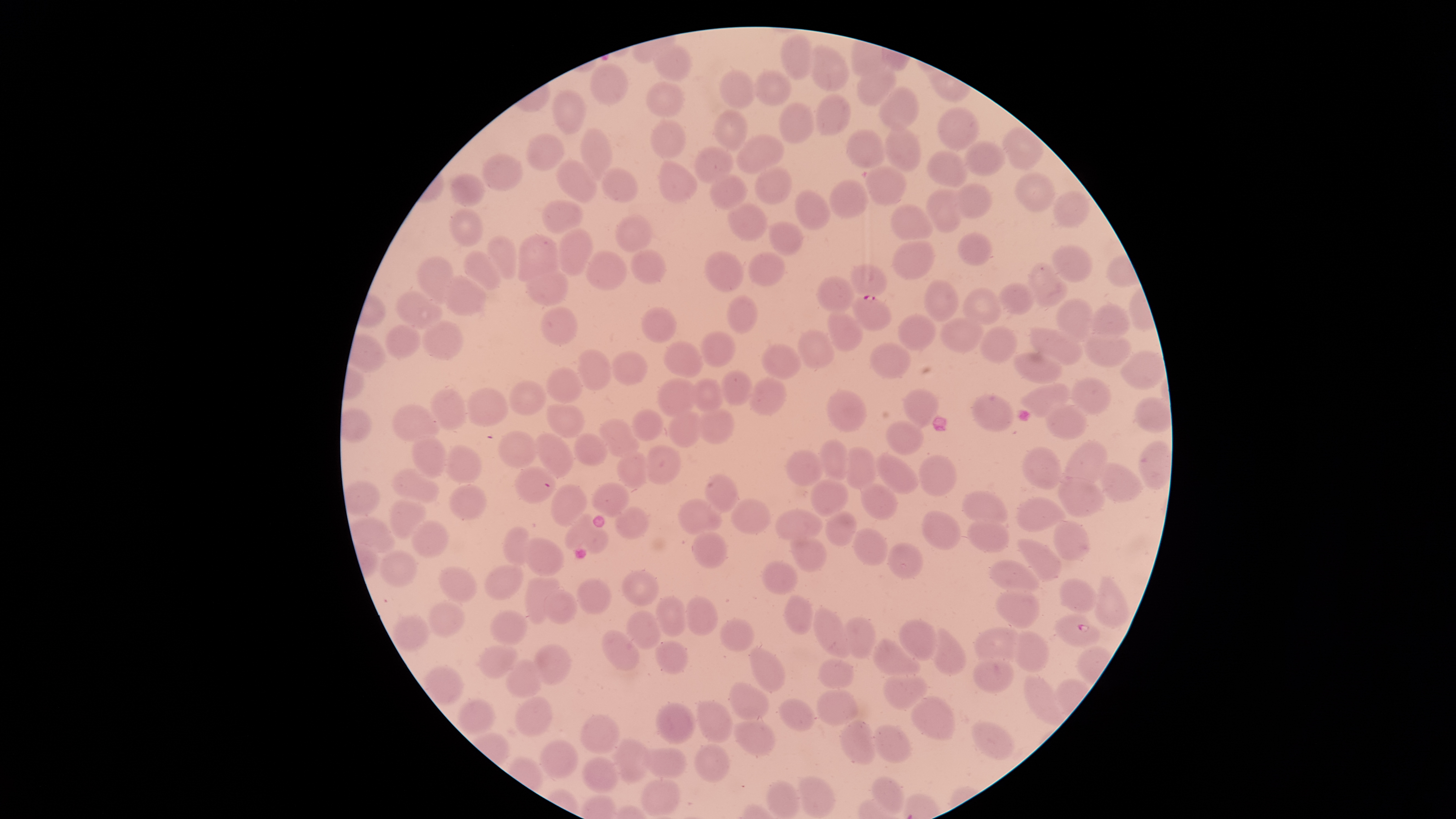
Approximate bounding boxes as {left, top, right, bottom} in pixels. Parasitized RBCs: {851, 295, 891, 331}, {1053, 613, 1101, 647}. Uninfected RBCs: {780, 33, 812, 80}, {652, 43, 692, 81}, {808, 46, 849, 90}, {590, 64, 628, 105}, {856, 64, 896, 107}, {754, 69, 792, 106}, {719, 70, 758, 108}, {646, 81, 684, 118}, {878, 86, 918, 130}, {551, 89, 586, 134}, {815, 94, 851, 135}, {778, 103, 815, 143}, {939, 107, 980, 149}, {713, 109, 747, 152}, {649, 120, 685, 159}, {886, 125, 921, 172}, {1003, 127, 1043, 169}, {580, 128, 612, 179}, {847, 129, 884, 169}, {526, 133, 564, 171}, {736, 134, 784, 174}, {963, 140, 1005, 175}, {693, 146, 733, 183}, {927, 150, 966, 187}, {481, 153, 523, 192}, {557, 159, 596, 203}, {657, 161, 697, 203}, {865, 166, 906, 205}, {754, 168, 791, 204}, {603, 169, 637, 204}, {1014, 172, 1056, 211}, {450, 173, 483, 206}, {710, 174, 746, 210}, {829, 179, 868, 218}, {955, 182, 992, 219}, {927, 189, 962, 233}, {795, 190, 830, 230}, {1053, 190, 1090, 228}, {541, 199, 583, 235}, {727, 203, 768, 241}, {891, 204, 932, 244}, {450, 208, 483, 247}, {616, 214, 653, 253}, {769, 222, 803, 257}, {553, 227, 594, 275}, {957, 232, 992, 265}, {515, 234, 560, 285}, {487, 235, 517, 278}, {892, 239, 935, 278}, {1052, 245, 1093, 282}, {703, 249, 743, 292}, {465, 250, 500, 293}, {631, 250, 666, 283}, {586, 251, 627, 292}, {747, 252, 785, 287}, {415, 256, 453, 298}, {848, 263, 888, 294}, {1025, 264, 1067, 307}, {527, 268, 569, 307}, {443, 274, 486, 317}, {817, 275, 854, 313}, {923, 279, 958, 321}, {997, 283, 1033, 315}, {962, 287, 1001, 326}, {395, 291, 441, 329}, {726, 295, 757, 334}, {1056, 298, 1094, 339}, {1092, 303, 1129, 340}, {540, 307, 577, 346}, {641, 307, 676, 343}, {825, 312, 862, 352}, {895, 314, 936, 349}, {941, 317, 983, 352}, {421, 320, 463, 360}, {384, 322, 420, 358}, {979, 326, 1016, 361}, {1029, 327, 1082, 365}, {798, 330, 833, 369}, {700, 331, 736, 366}, {1083, 332, 1131, 367}, {663, 341, 703, 378}, {870, 341, 910, 378}, {761, 345, 799, 379}, {578, 349, 612, 391}, {1012, 350, 1061, 386}, {1120, 350, 1164, 390}, {612, 351, 648, 385}, {547, 366, 582, 404}, {721, 370, 753, 405}, {692, 376, 721, 413}, {1074, 376, 1111, 415}, {657, 377, 698, 418}, {748, 378, 787, 414}, {509, 380, 546, 416}, {1025, 383, 1070, 418}, {430, 388, 466, 430}, {467, 388, 507, 427}, {904, 389, 938, 428}, {826, 390, 867, 432}, {972, 394, 1013, 431}, {1133, 397, 1169, 432}, {392, 403, 439, 442}, {547, 403, 584, 438}, {1046, 405, 1087, 439}, {699, 408, 734, 444}, {630, 409, 662, 440}, {668, 411, 704, 447}, {601, 418, 637, 458}, {886, 420, 925, 455}, {498, 430, 536, 469}, {573, 432, 607, 466}, {536, 434, 572, 477}, {413, 435, 446, 478}, {817, 440, 850, 482}, {1063, 440, 1108, 489}, {1140, 440, 1171, 490}, {645, 443, 681, 485}, {445, 446, 482, 483}, {843, 446, 876, 490}, {1022, 447, 1063, 489}, {616, 451, 650, 488}, {785, 451, 822, 486}, {875, 452, 919, 495}, {918, 454, 958, 497}, {1099, 463, 1141, 502}, {515, 466, 554, 505}, {391, 469, 439, 504}, {705, 474, 737, 512}, {1057, 477, 1106, 517}, {810, 478, 848, 515}, {593, 481, 629, 515}, {861, 483, 898, 521}, {447, 484, 487, 520}, {550, 484, 587, 526}, {962, 490, 1006, 525}, {390, 496, 427, 540}, {1017, 496, 1063, 532}, {678, 498, 722, 536}, {731, 498, 769, 533}, {615, 508, 649, 538}, {775, 509, 822, 542}, {920, 509, 961, 550}, {824, 510, 856, 547}, {564, 516, 608, 554}, {968, 518, 1010, 553}, {411, 520, 449, 560}, {1053, 520, 1089, 561}, {503, 526, 530, 566}, {852, 528, 890, 566}, {691, 531, 728, 568}, {789, 533, 827, 573}, {524, 537, 563, 576}, {1019, 539, 1062, 581}, {887, 542, 924, 579}, {379, 551, 418, 587}, {761, 559, 798, 596}, {990, 559, 1039, 595}, {486, 564, 522, 600}, {438, 566, 476, 603}, {621, 569, 659, 605}, {525, 576, 559, 625}, {576, 577, 612, 615}, {1058, 577, 1097, 613}, {1096, 582, 1129, 629}, {996, 589, 1040, 628}, {543, 591, 577, 625}, {784, 594, 812, 636}, {656, 596, 687, 636}, {686, 597, 718, 635}, {429, 601, 465, 638}, {812, 608, 852, 658}, {491, 610, 527, 646}, {627, 610, 661, 650}, {394, 614, 429, 651}, {844, 615, 874, 660}, {718, 617, 754, 652}, {899, 619, 940, 661}, {975, 626, 1022, 667}, {930, 628, 965, 675}, {601, 630, 639, 671}, {1012, 630, 1049, 670}, {873, 638, 921, 680}, {654, 640, 688, 673}, {478, 642, 517, 679}, {535, 643, 570, 684}, {749, 647, 785, 691}, {972, 657, 1014, 693}, {817, 658, 854, 691}, {505, 659, 543, 696}, {426, 665, 462, 703}, {883, 671, 928, 709}, {1024, 674, 1061, 726}, {729, 682, 769, 720}, {816, 689, 859, 725}, {516, 696, 553, 736}, {779, 698, 814, 732}, {911, 698, 956, 739}, {458, 699, 496, 735}, {697, 699, 733, 743}, {655, 702, 697, 743}, {580, 713, 619, 754}, {733, 720, 775, 757}, {840, 720, 877, 765}, {972, 720, 1015, 759}, {872, 724, 911, 762}, {612, 738, 651, 783}, {539, 739, 578, 780}, {694, 743, 729, 782}, {642, 746, 686, 779}, {582, 757, 619, 793}, {798, 776, 834, 817}, {873, 776, 904, 813}, {641, 779, 680, 817}, {767, 781, 799, 819}. Circular visible region. Single field of view. Species: Plasmodium falciparum. Photographed with a smartphone camera through the microscope eyepiece. Giemsa stain. Presence: malaria parasites detected. Thin smear of blood. Image is 1456×819 pixels.